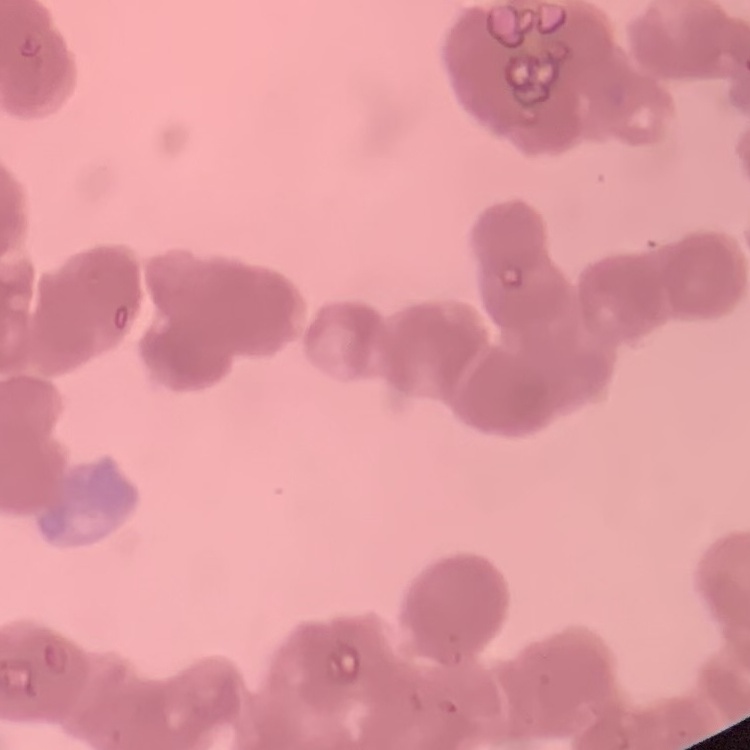
Summary:
  - Erythrocyte morphology: rouleaux formation
  - Preparation: thin peripheral smear
  - Stain: Field's or Giemsa
  - Image type: square crop of a larger photomicrograph